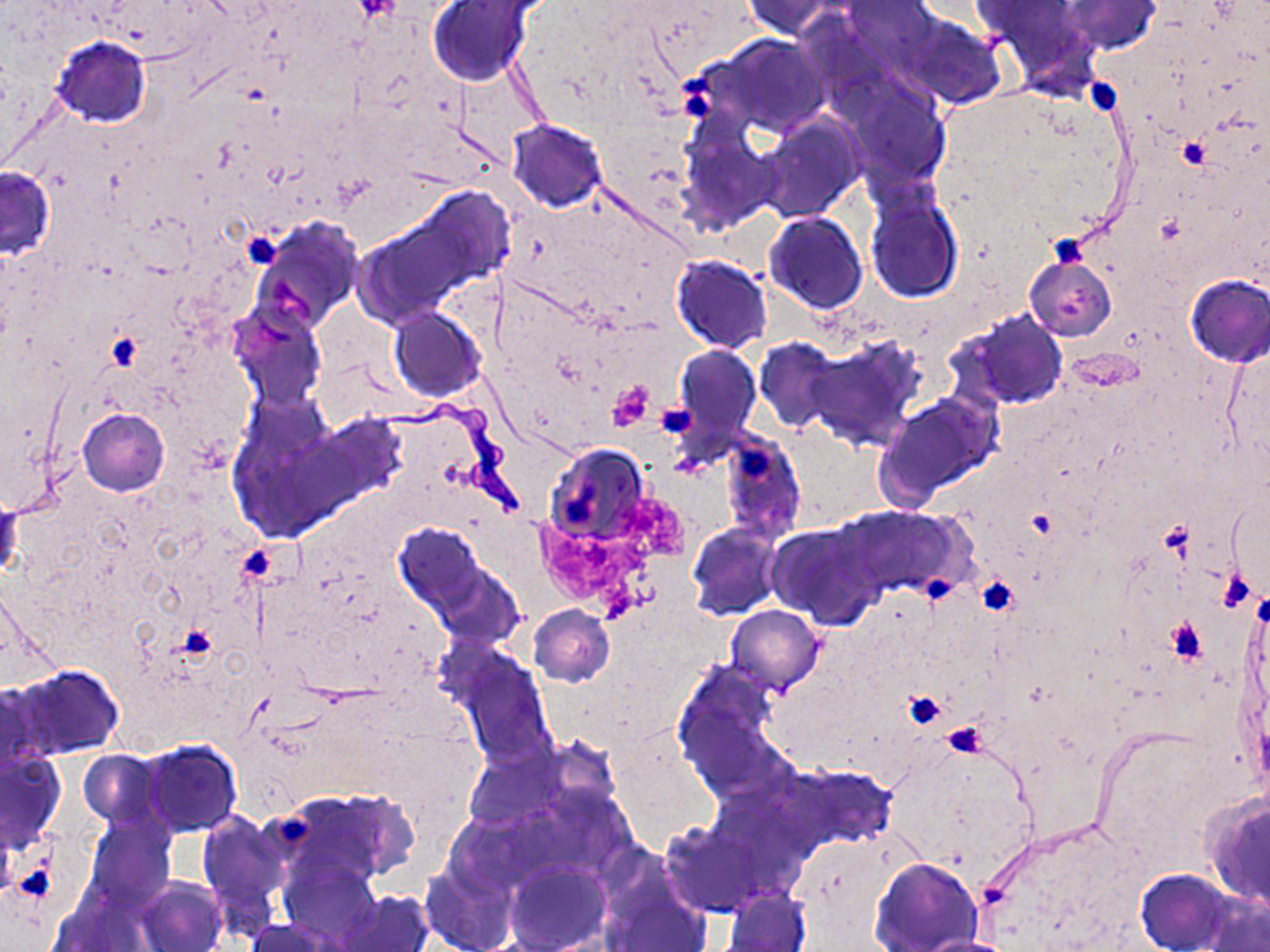 Approximate bounding boxes as (x1, y1, x2, y2) in pixels. Uninfected red blood cell locations: (427, 0, 535, 87), (741, 0, 850, 38), (845, 1, 943, 70), (1061, 1, 1163, 54), (905, 18, 1005, 107), (52, 35, 151, 127), (716, 35, 830, 137), (849, 85, 949, 187), (757, 118, 860, 222), (506, 119, 608, 212), (676, 130, 774, 230), (0, 163, 56, 263), (865, 192, 964, 303), (352, 194, 504, 328), (765, 211, 869, 314), (251, 220, 364, 335), (1023, 253, 1116, 342), (671, 254, 773, 354), (1184, 273, 1270, 367), (228, 303, 328, 412), (388, 306, 486, 401), (951, 309, 1069, 411), (755, 337, 846, 433), (806, 337, 923, 453), (1220, 341, 1270, 476), (672, 345, 762, 450), (873, 392, 1003, 509), (77, 408, 170, 496), (720, 432, 807, 544), (544, 444, 652, 546), (1226, 482, 1270, 599), (1, 495, 20, 579), (834, 504, 965, 603), (392, 522, 492, 620), (687, 522, 784, 621), (766, 523, 879, 627), (1240, 580, 1268, 778), (529, 605, 615, 686), (725, 605, 825, 694), (450, 646, 558, 769), (671, 661, 789, 795), (12, 663, 125, 760), (1088, 724, 1240, 853), (137, 740, 242, 838), (0, 749, 66, 850), (76, 749, 164, 828), (783, 763, 897, 848), (1201, 791, 1270, 911), (86, 813, 174, 908), (199, 815, 289, 924), (661, 822, 763, 917), (870, 856, 983, 951), (284, 858, 379, 948), (422, 859, 516, 952), (506, 862, 610, 951), (1135, 868, 1236, 952), (134, 877, 227, 952), (604, 887, 712, 951), (723, 887, 811, 952), (339, 890, 435, 952), (1201, 895, 1270, 952), (243, 918, 342, 951), (909, 936, 1023, 952). Platelet locations: (353, 0, 399, 23), (673, 66, 712, 98), (1085, 74, 1127, 116), (677, 93, 718, 120), (1177, 137, 1212, 169), (241, 232, 282, 269), (1052, 232, 1088, 271), (104, 331, 142, 371), (608, 381, 655, 428), (653, 404, 696, 439), (734, 442, 779, 478), (563, 489, 597, 523), (240, 546, 271, 578), (927, 574, 955, 603), (975, 575, 1017, 615), (1165, 615, 1208, 667), (176, 624, 217, 662), (903, 689, 947, 731), (941, 724, 985, 756), (275, 816, 316, 843), (18, 860, 54, 897). Trypanosoma brucei locations: (374, 399, 533, 525). Slide-level diagnosis: Trypanosoma brucei. Image is 1270×952 pixels. May-Grünwald-Giemsa-stained preparation. Thin blood film. 1000x magnification. Light microscopy. One field of a larger specimen.